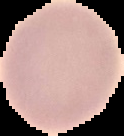 Image is 124×136 pixels. The area outside the segmented cell region is set to black. From a thin blood film. Malaria status: uninfected.